Identify the parasite.
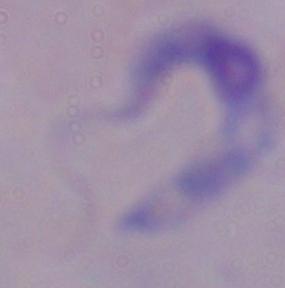
This is a trypanosome.

Photomicrograph. Captured at 1000x magnification.